Identify the blood parasite species.
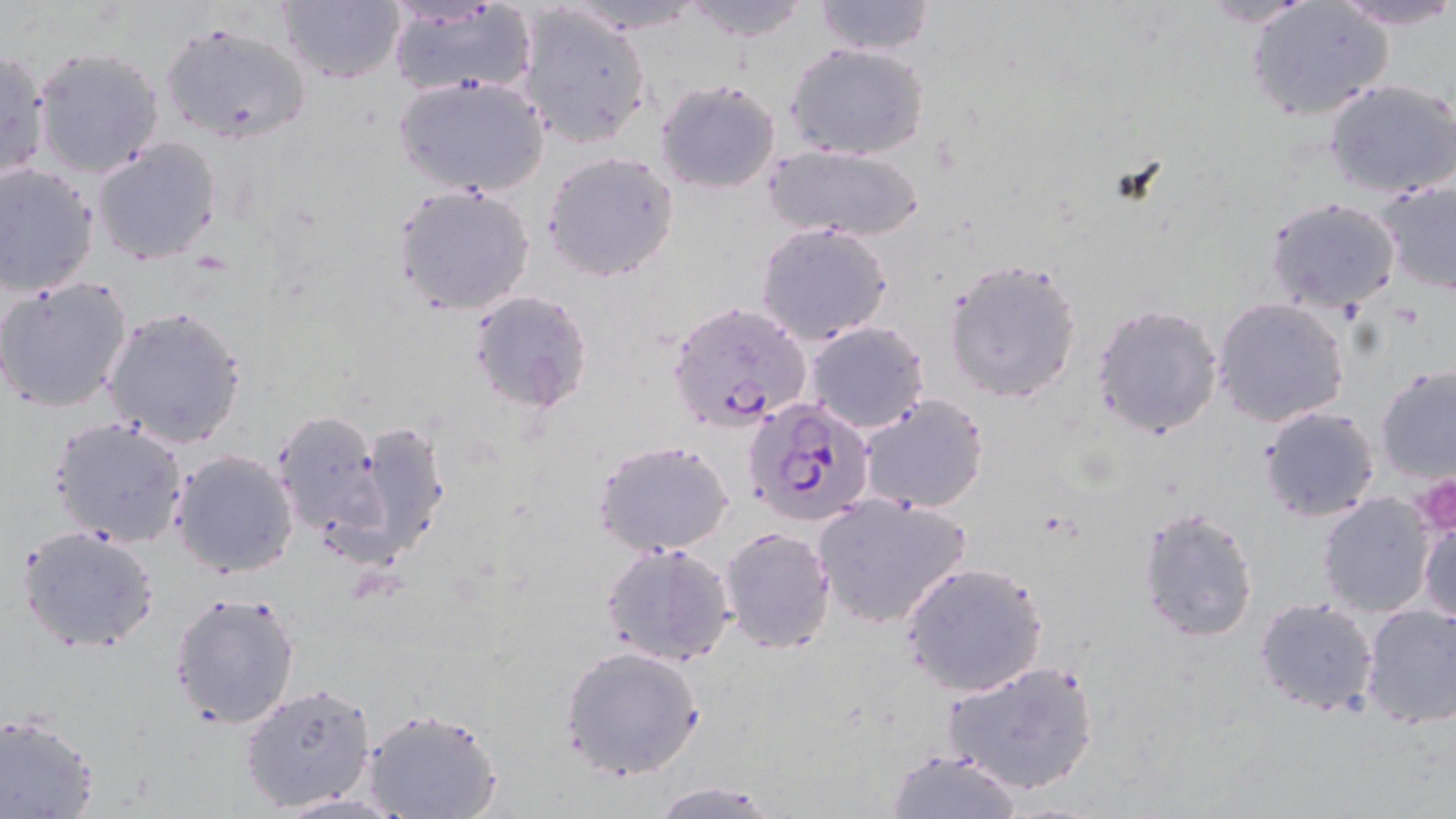
Plasmodium falciparum.

Summary:
  - Coordinate format: approximate bounding boxes as named x1/y1/x2/y2 corners in pixels
  - Platelet locations: (x1=1408, y1=473, x2=1456, y2=538)
  - Uninfected red blood cell locations: (x1=679, y1=0, x2=814, y2=43), (x1=812, y1=0, x2=937, y2=55), (x1=1194, y1=0, x2=1318, y2=27), (x1=1330, y1=0, x2=1455, y2=31), (x1=276, y1=1, x2=405, y2=85), (x1=384, y1=3, x2=536, y2=100), (x1=1244, y1=3, x2=1392, y2=120), (x1=520, y1=7, x2=650, y2=148), (x1=160, y1=21, x2=314, y2=145), (x1=788, y1=43, x2=930, y2=161), (x1=33, y1=47, x2=165, y2=178), (x1=0, y1=48, x2=50, y2=182), (x1=394, y1=74, x2=550, y2=198), (x1=654, y1=78, x2=781, y2=192), (x1=1324, y1=80, x2=1456, y2=200), (x1=92, y1=136, x2=224, y2=266), (x1=766, y1=143, x2=925, y2=241), (x1=542, y1=150, x2=680, y2=281), (x1=0, y1=163, x2=99, y2=296), (x1=1374, y1=178, x2=1456, y2=295), (x1=393, y1=184, x2=536, y2=317), (x1=1263, y1=197, x2=1403, y2=314), (x1=754, y1=222, x2=894, y2=347), (x1=942, y1=257, x2=1084, y2=404), (x1=0, y1=276, x2=134, y2=415), (x1=470, y1=290, x2=591, y2=413), (x1=1213, y1=298, x2=1350, y2=426), (x1=1090, y1=302, x2=1224, y2=439), (x1=100, y1=306, x2=247, y2=449), (x1=805, y1=321, x2=930, y2=433), (x1=1375, y1=364, x2=1456, y2=483), (x1=858, y1=393, x2=989, y2=515), (x1=1257, y1=406, x2=1381, y2=521), (x1=271, y1=408, x2=389, y2=542), (x1=50, y1=416, x2=191, y2=548), (x1=347, y1=420, x2=450, y2=557), (x1=594, y1=439, x2=735, y2=554), (x1=170, y1=448, x2=299, y2=577), (x1=1316, y1=492, x2=1438, y2=619), (x1=811, y1=495, x2=973, y2=630), (x1=1134, y1=505, x2=1261, y2=645), (x1=1418, y1=515, x2=1456, y2=624), (x1=719, y1=526, x2=836, y2=652), (x1=18, y1=527, x2=159, y2=652), (x1=598, y1=540, x2=737, y2=667), (x1=900, y1=562, x2=1048, y2=699), (x1=168, y1=590, x2=303, y2=729), (x1=1254, y1=598, x2=1379, y2=716), (x1=1360, y1=604, x2=1456, y2=731), (x1=561, y1=645, x2=705, y2=780), (x1=943, y1=659, x2=1100, y2=795), (x1=239, y1=682, x2=377, y2=813), (x1=360, y1=705, x2=503, y2=819), (x1=0, y1=714, x2=100, y2=819), (x1=886, y1=748, x2=1023, y2=819), (x1=650, y1=781, x2=775, y2=818)
  - Plasmodium falciparum-infected red blood cell locations: (x1=666, y1=300, x2=811, y2=433), (x1=746, y1=398, x2=875, y2=527)
  - Preparation: thin blood smear
  - Magnification: 1000x
  - Stain: May-Grünwald-Giemsa
  - Modality: optical microscopy
  - Image size: 1456×819 pixels
  - Field of view: single